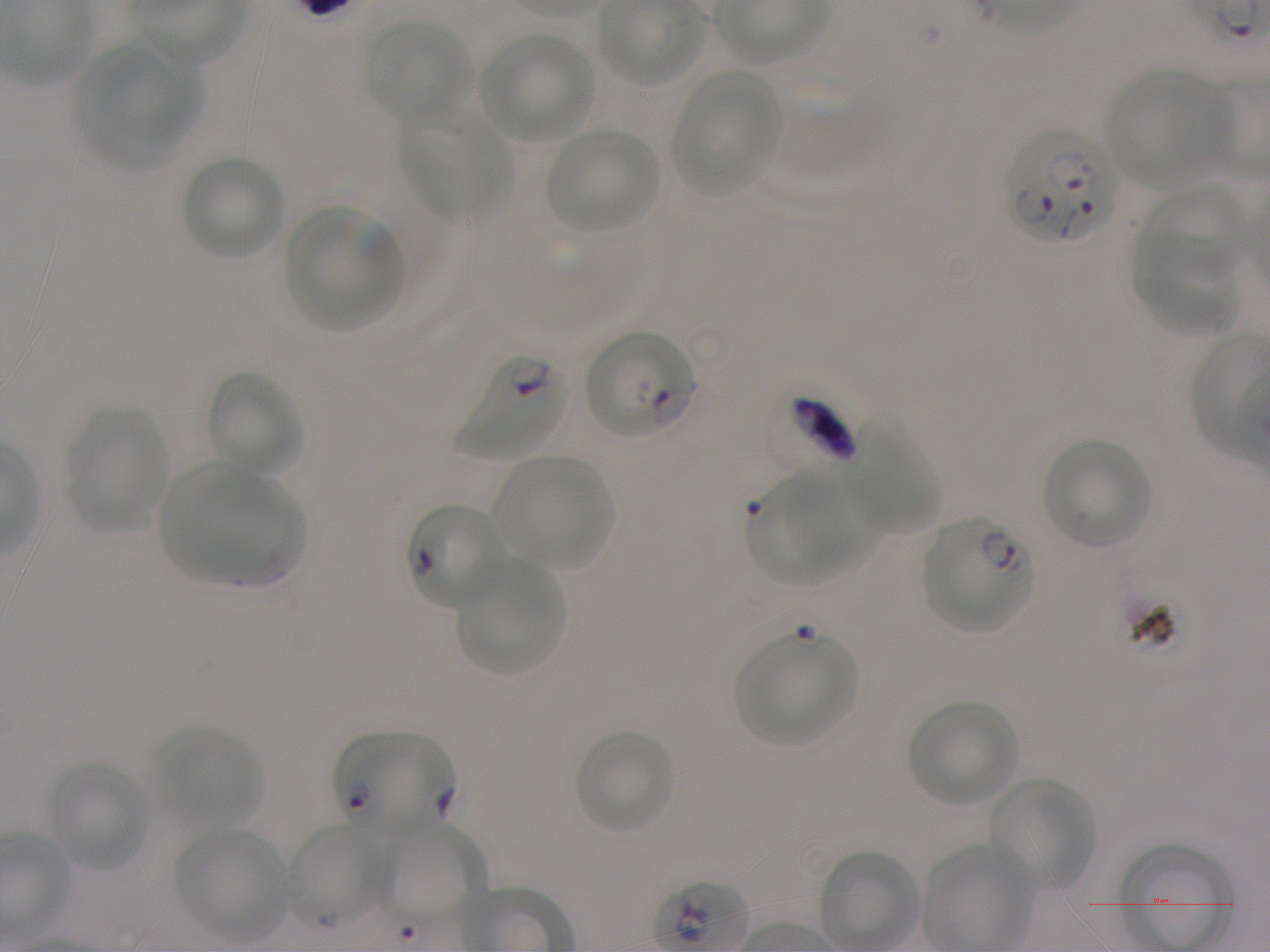

Approximate bounding boxes as (x1, y1, x2, y2) in pixels. Not every red blood cell is marked. A life-cycle stage — or a range of stages, where the recorded stages span more than one — follows each staged infected red blood cell. Locations of infected red blood cells: (1005, 130, 1118, 244); (582, 330, 696, 440) ring; (455, 353, 568, 461); (775, 392, 857, 466); (406, 503, 506, 609); (923, 518, 1033, 634) ring; (336, 732, 453, 839). Locations of uninfected red blood cells: (365, 20, 470, 125), (478, 32, 596, 142), (100, 39, 204, 146), (79, 44, 185, 164), (1106, 70, 1230, 189), (673, 72, 781, 198), (397, 102, 507, 221), (545, 127, 658, 233), (181, 156, 285, 260), (1145, 184, 1249, 279), (285, 206, 403, 331), (1133, 231, 1240, 335), (204, 370, 306, 478), (66, 409, 168, 532), (850, 409, 939, 533), (1043, 439, 1152, 549), (495, 456, 614, 571), (168, 466, 269, 585), (786, 466, 887, 573), (746, 472, 860, 584), (194, 474, 308, 585), (455, 561, 564, 675), (733, 633, 858, 745), (907, 699, 1019, 807), (153, 728, 262, 829), (572, 728, 675, 835), (47, 762, 152, 870), (989, 778, 1094, 893), (381, 821, 487, 926), (286, 823, 385, 930), (176, 828, 290, 941). Single field of view. Oil immersion, 100x objective (numerical aperture 1.25). Donor blood group A+. Image is 1270×952 pixels. Giemsa stain. Thin blood film. P. falciparum strain NF54 maintained in static in-vitro culture.